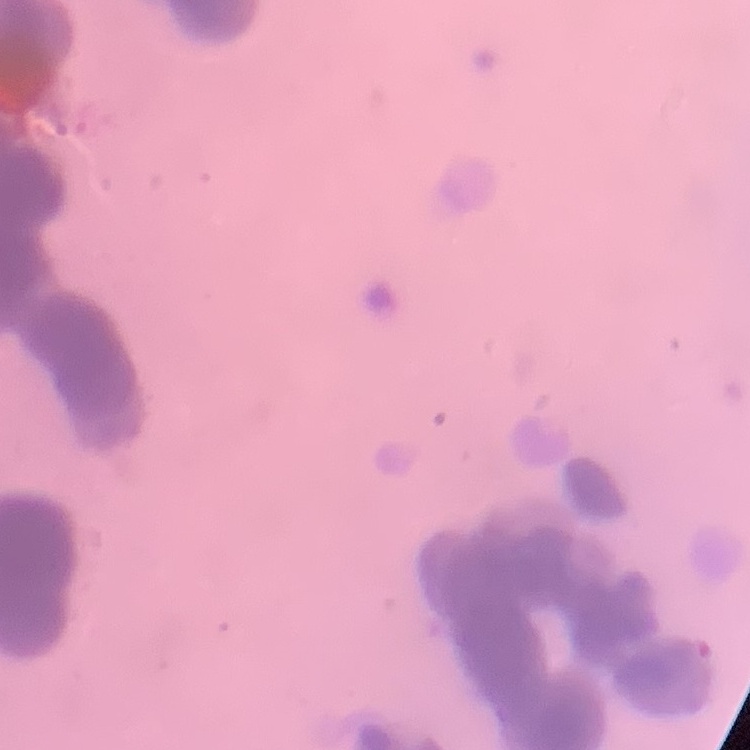
Summary:
  - Erythrocyte morphology: rouleaux formation
  - Preparation: thin blood smear
  - Stain: Field's or Giemsa
  - Image type: one tile cut from a larger photomicrograph